State the blood parasite species.
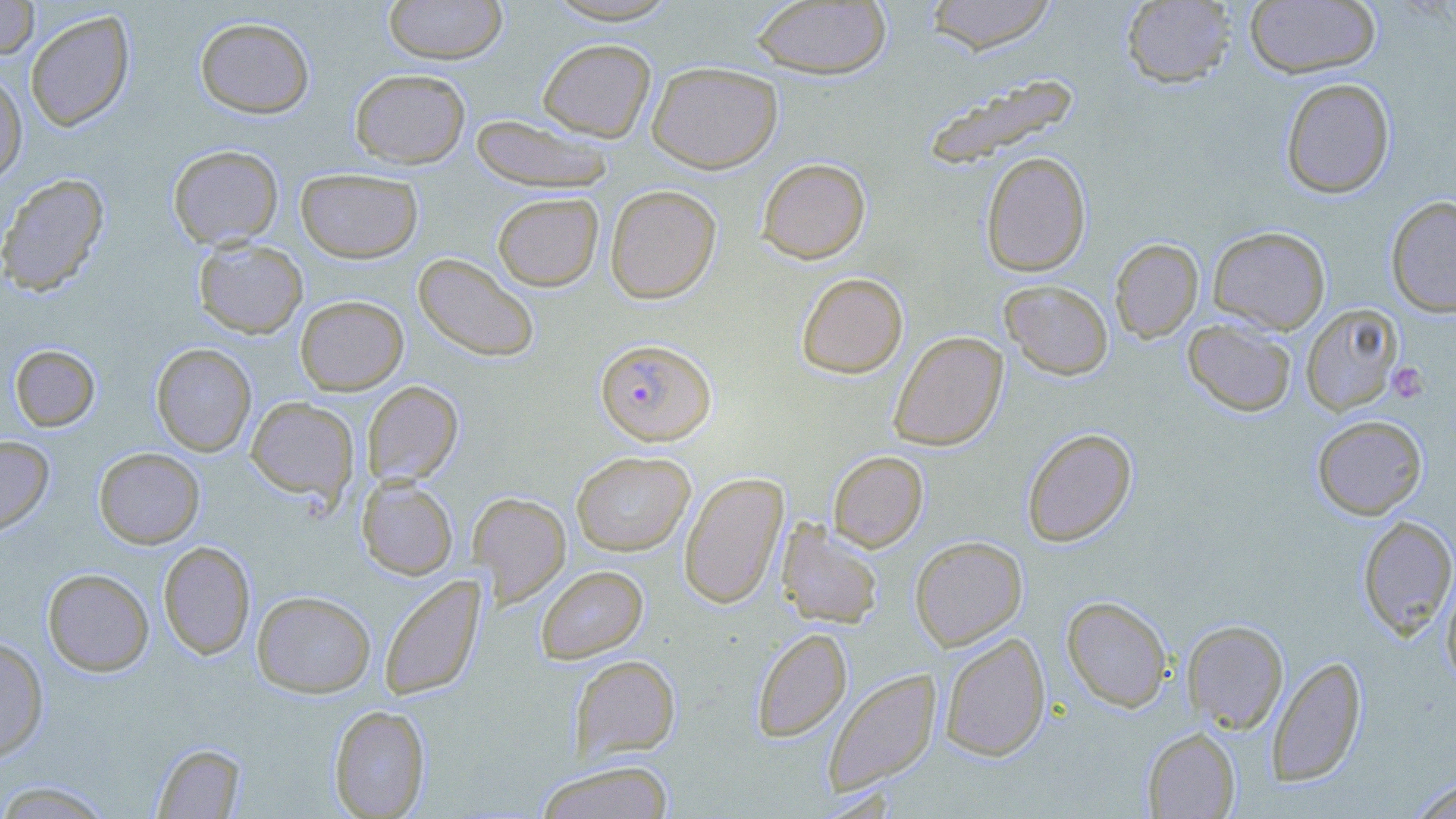

Plasmodium falciparum.

Summary:
  - Coordinate format: approximate bounding boxes as [x1, y1, x2, y2] in pixels
  - Platelet locations: [1386, 362, 1428, 403]
  - Plasmodium falciparum-infected red blood cell locations: [595, 339, 717, 445]
  - Uninfected red blood cell locations: [0, 0, 39, 59], [383, 0, 507, 64], [543, 0, 683, 26], [925, 0, 1057, 54], [1120, 0, 1237, 88], [751, 1, 892, 79], [1245, 1, 1381, 78], [25, 10, 135, 131], [195, 16, 315, 118], [537, 38, 656, 142], [647, 61, 782, 173], [350, 68, 470, 169], [0, 70, 28, 184], [922, 73, 1080, 169], [1280, 78, 1395, 199], [471, 114, 614, 193], [167, 144, 283, 249], [980, 151, 1091, 277], [757, 158, 871, 264], [295, 167, 423, 263], [0, 173, 109, 296], [605, 184, 722, 304], [492, 192, 603, 291], [1385, 195, 1456, 318], [1208, 226, 1331, 335], [193, 238, 308, 339], [1110, 238, 1203, 342], [413, 252, 539, 363], [797, 272, 908, 378], [1000, 280, 1114, 380], [295, 295, 408, 395], [1301, 304, 1403, 415], [1182, 318, 1297, 417], [889, 331, 1008, 451], [151, 343, 256, 456], [10, 344, 100, 432], [362, 380, 463, 486], [245, 397, 359, 503], [1311, 415, 1427, 519], [1021, 427, 1137, 547], [0, 435, 53, 535], [94, 447, 205, 548], [571, 451, 695, 556], [828, 451, 928, 552], [678, 471, 788, 609], [356, 477, 458, 580], [468, 492, 571, 606], [1358, 515, 1456, 640], [776, 520, 883, 629], [910, 536, 1027, 650], [158, 540, 255, 660], [535, 565, 648, 664], [42, 568, 154, 676], [1441, 568, 1456, 688], [379, 574, 486, 701], [252, 590, 376, 697], [1061, 595, 1173, 712], [1182, 619, 1289, 734], [751, 628, 852, 742], [939, 631, 1051, 761], [0, 637, 49, 763], [570, 654, 681, 760], [1266, 655, 1367, 787], [823, 668, 942, 797], [328, 704, 430, 818], [1142, 726, 1241, 818], [152, 742, 246, 818], [533, 760, 675, 819], [1407, 777, 1456, 819], [0, 779, 114, 818]
  - Stain: May-Grünwald-Giemsa
  - Field of view: one of a larger specimen
  - Magnification: 1000x
  - Modality: light microscopy
  - Preparation: thin blood smear
  - Image size: 1456×819 pixels